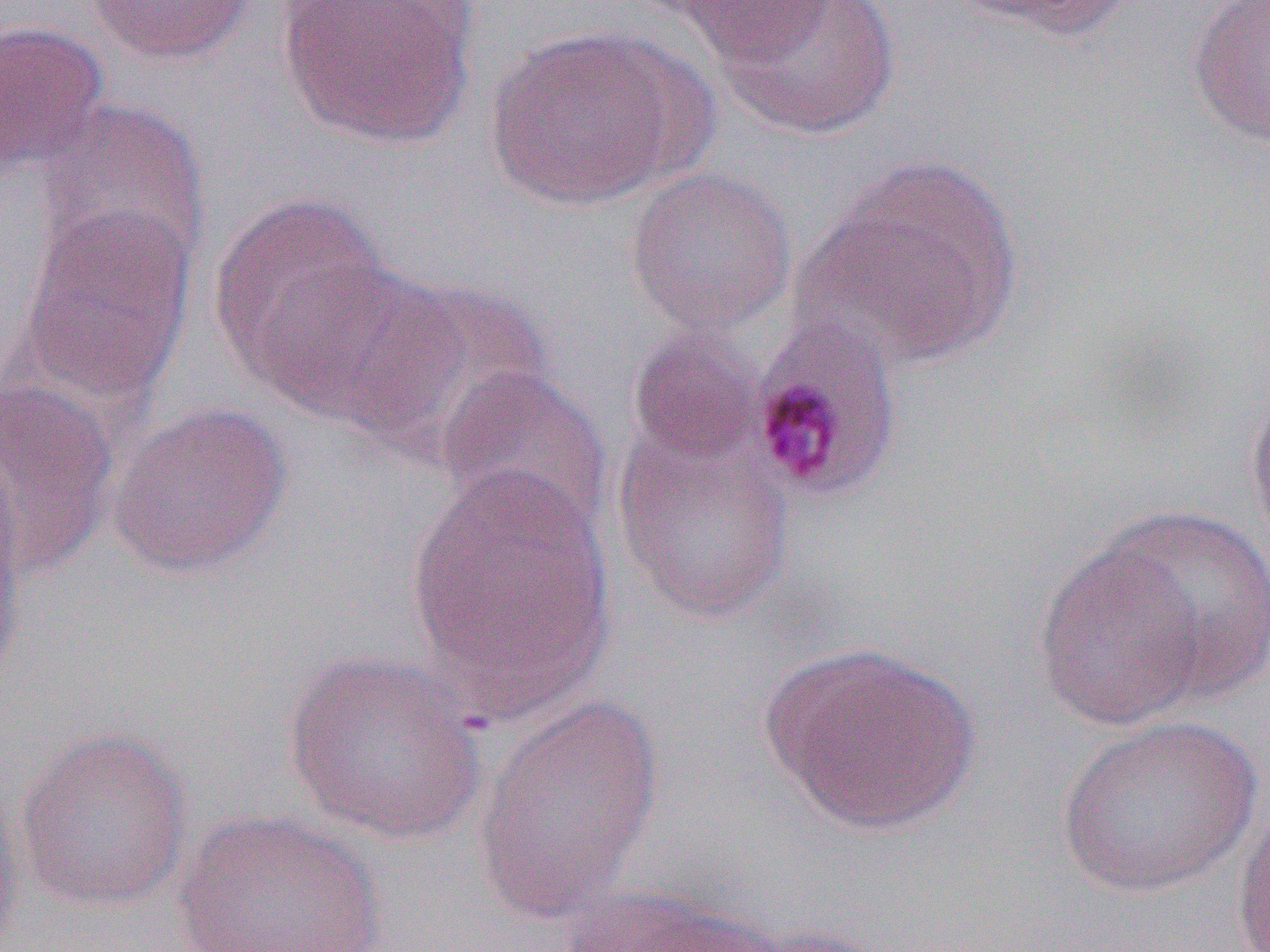 Approximate bounding boxes as [x1, y1, x2, y2] in pixels. Plasmodium malariae-infected red blood cell locations: [748, 317, 904, 504]. Uninfected red blood cell locations: [84, 0, 257, 66], [944, 0, 1139, 41], [1186, 0, 1270, 147], [276, 1, 479, 149], [667, 1, 839, 68], [717, 1, 901, 140], [0, 20, 109, 178], [481, 24, 697, 211], [35, 97, 209, 277], [811, 154, 1026, 369], [624, 166, 798, 338], [209, 191, 396, 391], [18, 204, 196, 410], [256, 257, 446, 431], [353, 278, 554, 464], [627, 327, 765, 468], [435, 365, 611, 536], [0, 378, 118, 577], [1245, 389, 1270, 570], [105, 400, 292, 580], [610, 426, 797, 626], [404, 460, 619, 721], [1095, 503, 1270, 706], [0, 506, 26, 689], [1030, 538, 1214, 733], [759, 639, 981, 837], [282, 650, 491, 845], [474, 696, 665, 920], [1055, 713, 1262, 899], [13, 726, 193, 912], [0, 773, 25, 951], [1232, 796, 1270, 952], [171, 809, 389, 952], [558, 885, 801, 952], [727, 925, 890, 952]. Slide-level diagnosis: Plasmodium malariae. Light microscopy. Thin blood film. 1000x magnification. Image is 1270×952 pixels. One field of a larger specimen.